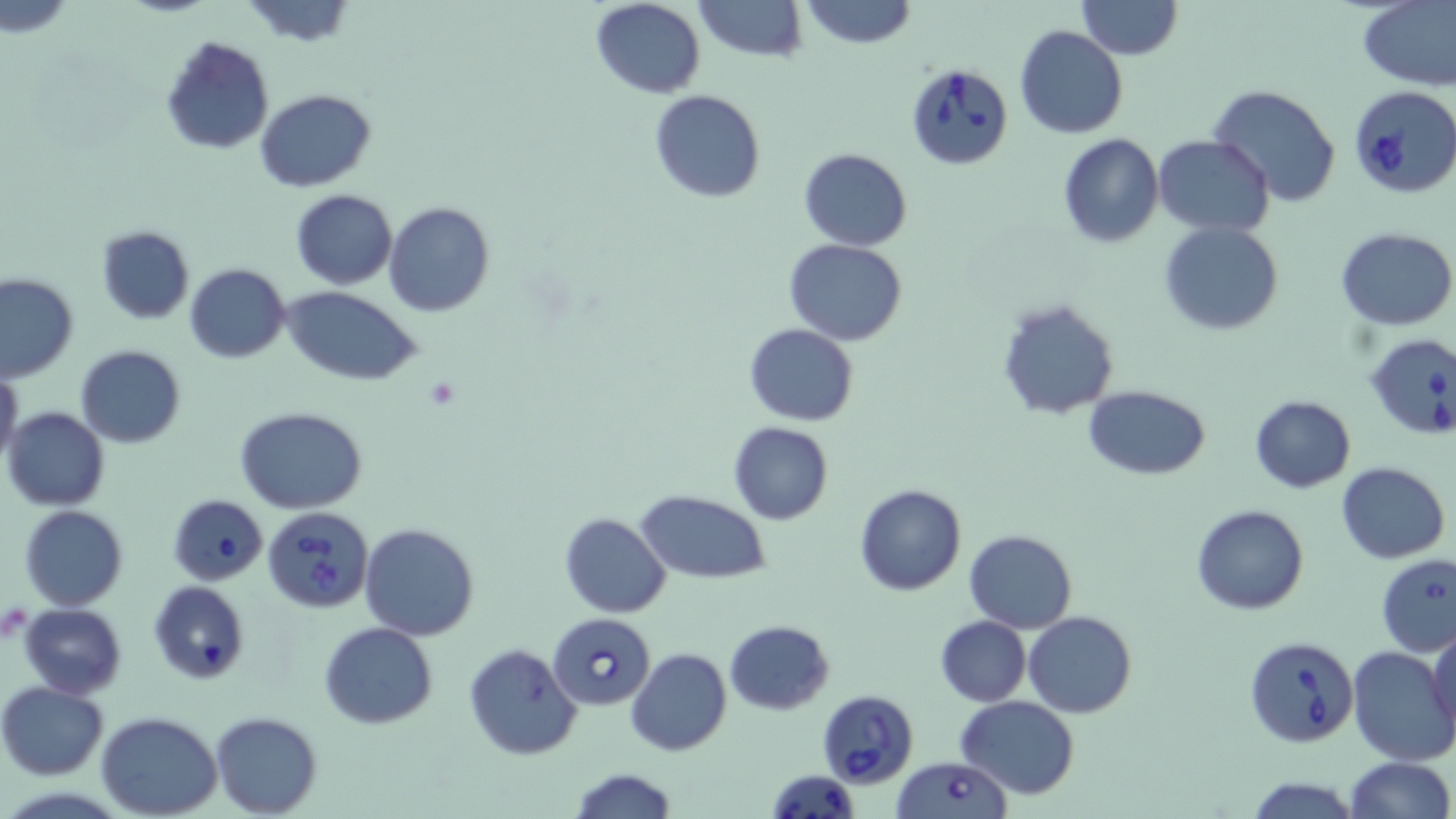

slide-level diagnosis = Babesia divergens
platelet locations = approximate bounding boxes as [x1, y1, x2, y2] in pixels: [425, 378, 461, 411]
stain = May-Grünwald-Giemsa
field of view = one of a larger specimen
image size = 1456×819 pixels
preparation = thin blood smear
magnification = 1000x
Babesia divergens-infected red blood cell locations = approximate bounding boxes as [x1, y1, x2, y2] in pixels: [906, 66, 1012, 171], [1349, 86, 1456, 198], [1363, 333, 1456, 440], [168, 494, 268, 586], [263, 506, 375, 614], [549, 612, 656, 709], [1242, 634, 1358, 747], [817, 691, 918, 787], [890, 757, 1013, 818], [766, 770, 860, 818]
uninfected red blood cell locations = approximate bounding boxes as [x1, y1, x2, y2] in pixels: [240, 0, 359, 49], [591, 0, 706, 98], [694, 0, 806, 61], [798, 0, 916, 48], [1077, 0, 1181, 60], [1357, 1, 1455, 90], [1014, 24, 1128, 138], [158, 35, 274, 155], [1209, 85, 1342, 208], [255, 88, 376, 192], [649, 90, 766, 203], [1057, 133, 1164, 247], [1152, 134, 1275, 236], [798, 147, 914, 251], [290, 189, 396, 290], [385, 202, 495, 317], [1159, 221, 1283, 336], [95, 225, 195, 325], [1336, 228, 1456, 329], [784, 238, 908, 345], [185, 263, 291, 363], [0, 272, 78, 383], [283, 289, 422, 384], [996, 297, 1120, 421], [743, 323, 858, 426], [75, 345, 187, 448], [0, 367, 24, 472], [1084, 386, 1211, 479], [1249, 394, 1356, 493], [4, 406, 110, 511], [235, 408, 369, 512], [727, 421, 833, 526], [1337, 463, 1450, 563], [855, 484, 965, 596], [635, 491, 771, 582], [20, 505, 127, 611], [1192, 505, 1309, 615], [559, 513, 670, 618], [359, 524, 482, 640], [964, 529, 1077, 633], [1375, 554, 1456, 658], [149, 580, 249, 684], [20, 603, 126, 697], [1024, 611, 1136, 718], [936, 616, 1031, 706], [724, 619, 834, 714], [319, 621, 437, 729], [1429, 625, 1456, 741], [462, 642, 583, 761], [1347, 646, 1456, 765], [626, 648, 731, 758], [0, 681, 110, 780], [955, 696, 1081, 799], [97, 711, 221, 818], [210, 711, 322, 817], [1342, 756, 1453, 819], [568, 768, 679, 819], [1244, 775, 1361, 819]
modality = light microscopy